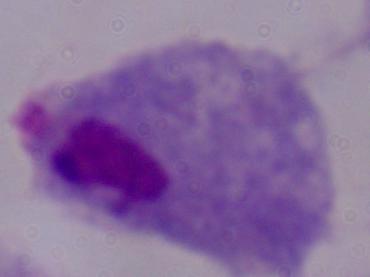

Summary:
  - Magnification: 1000x
  - Identification: trichomonad
  - Modality: micrograph